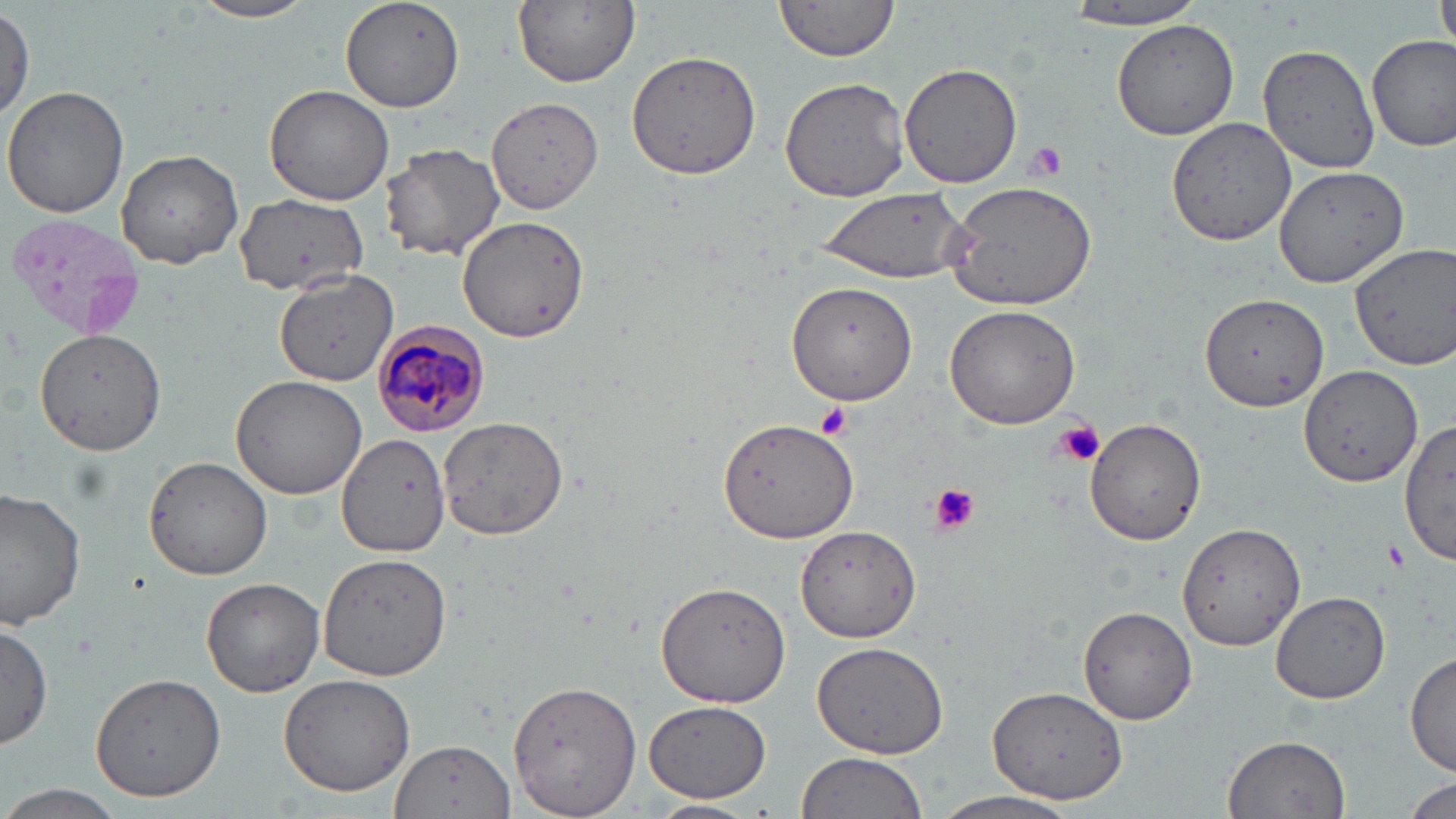
Approximate bounding boxes as [x1, y1, x2, y2] in pixels. Platelet locations: [1023, 141, 1067, 182], [816, 403, 852, 439], [1052, 420, 1107, 468], [927, 482, 979, 535], [1386, 540, 1407, 572]. Uninfected red blood cell locations: [190, 0, 320, 23], [339, 0, 466, 113], [511, 0, 640, 88], [771, 0, 903, 63], [1062, 0, 1211, 30], [1434, 0, 1456, 67], [0, 3, 35, 122], [1111, 21, 1240, 139], [1368, 34, 1455, 150], [1258, 42, 1380, 174], [624, 49, 763, 178], [898, 62, 1021, 189], [779, 77, 913, 205], [264, 84, 397, 206], [3, 86, 130, 220], [485, 95, 605, 214], [1166, 117, 1300, 248], [379, 143, 506, 260], [116, 148, 244, 269], [1272, 163, 1408, 287], [941, 178, 1100, 311], [814, 186, 972, 283], [236, 196, 365, 297], [457, 215, 588, 341], [1353, 244, 1456, 370], [274, 268, 399, 385], [785, 281, 916, 405], [1200, 292, 1329, 413], [943, 303, 1081, 429], [32, 325, 166, 456], [1298, 363, 1423, 488], [231, 373, 369, 501], [436, 415, 570, 541], [719, 416, 858, 545], [1400, 417, 1456, 566], [1086, 418, 1207, 545], [338, 434, 452, 556], [143, 455, 277, 581], [0, 485, 84, 630], [1176, 521, 1305, 652], [796, 525, 922, 644], [320, 551, 452, 682], [201, 578, 325, 698], [655, 580, 789, 708], [1271, 591, 1390, 704], [1079, 606, 1198, 725], [0, 623, 52, 750], [809, 638, 951, 759], [1407, 648, 1455, 779], [88, 671, 224, 801], [277, 673, 417, 795], [510, 678, 644, 818], [987, 683, 1129, 806], [645, 700, 771, 802], [1223, 734, 1350, 818], [390, 736, 514, 816], [795, 754, 928, 819], [1401, 780, 1456, 819], [2, 786, 127, 818], [926, 791, 1082, 819], [645, 800, 759, 819]. Plasmodium malariae-infected red blood cell locations: [371, 322, 493, 435]. Slide-level diagnosis: Plasmodium malariae. May-Grünwald-Giemsa-stained preparation. Thin blood film. 1000x magnification. Image is 1456×819 pixels. Single field of view. Optical microscopy.